Assess this cell for malaria.
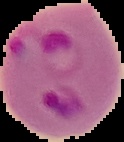

It is parasitized.

image size = 124×142 pixels
preparation = thin blood film
image type = segmented cell region on a black background